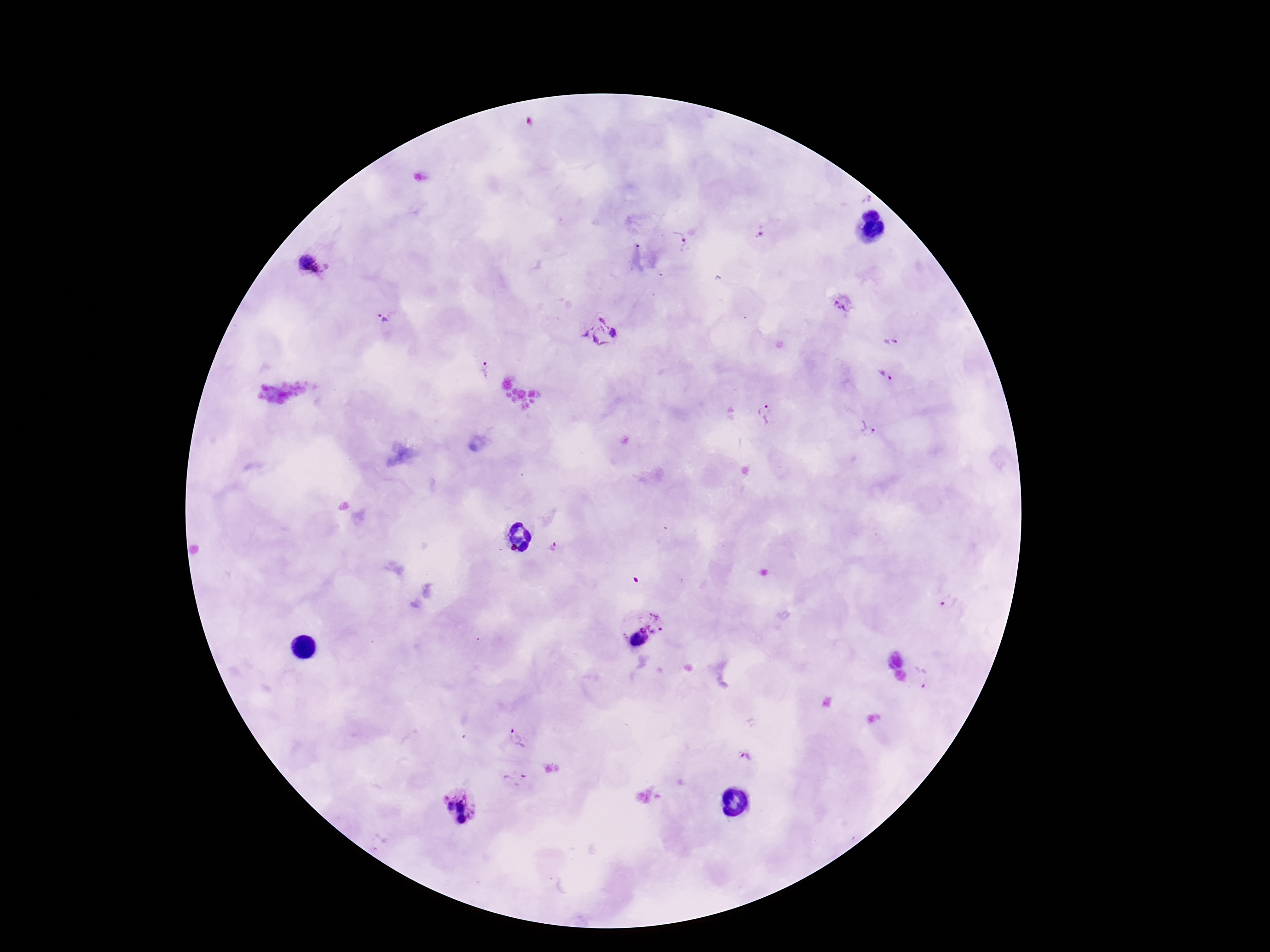
Plasmodium parasite locations = approximate object centers, in pixels from the top-left corner: (x=760, y=232), (x=679, y=239), (x=313, y=264), (x=843, y=303), (x=386, y=316), (x=601, y=332), (x=893, y=340), (x=483, y=369), (x=885, y=375), (x=764, y=414), (x=865, y=429), (x=553, y=546), (x=948, y=602), (x=641, y=626), (x=921, y=677), (x=517, y=740), (x=744, y=756), (x=515, y=778), (x=461, y=808)
image size = 1270×952 pixels
patient malaria status = infected
magnification = 100x
preparation = thick peripheral-blood smear
field of view = single
stain = Giemsa
capture = smartphone camera through the microscope eyepiece